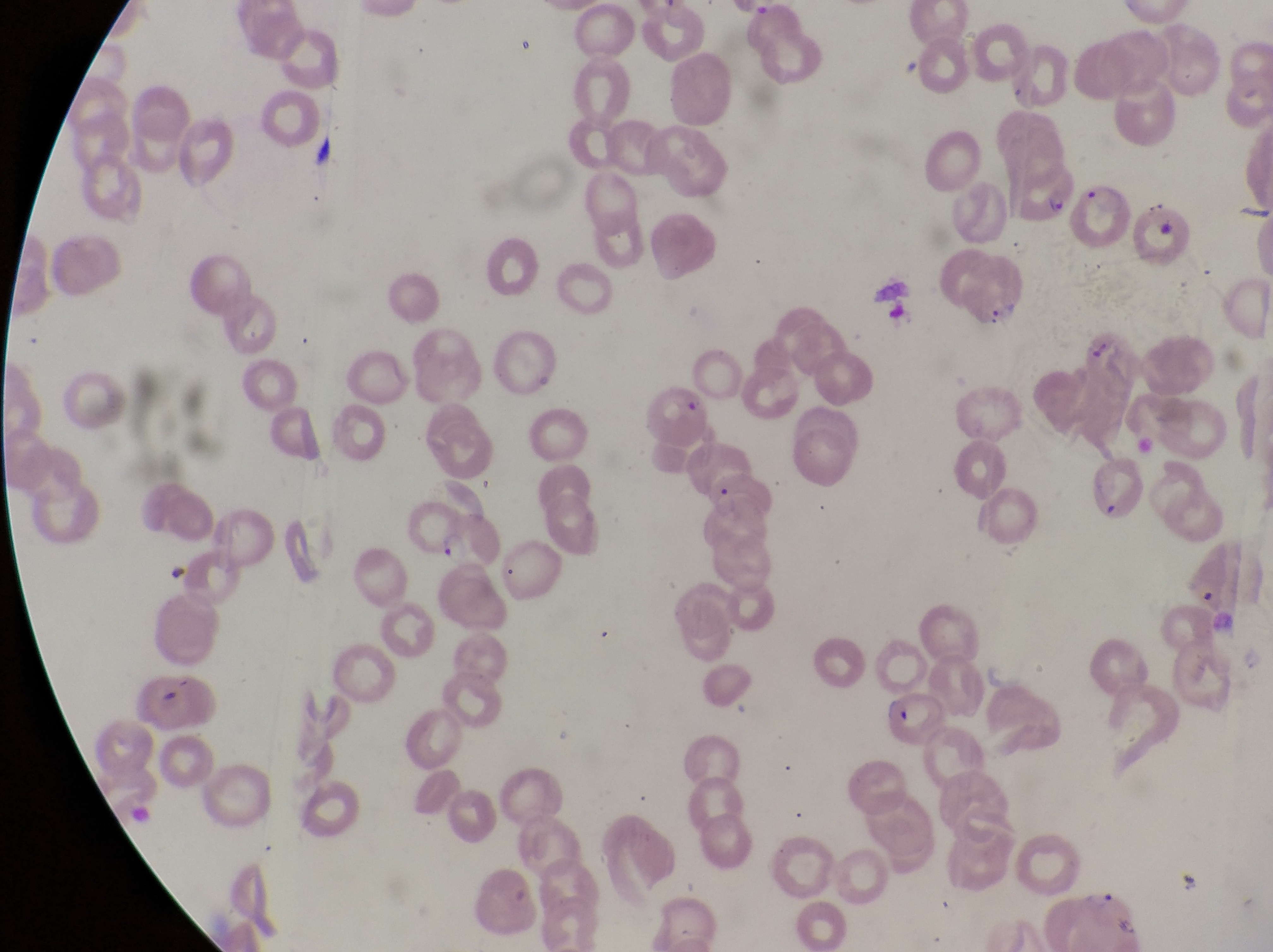
Approximate bounding boxes as (left, top, right, bottom) in pixels.
Summary:
  - Parasitised red blood cell locations: (1011, 158, 1081, 225), (1081, 180, 1138, 250), (961, 248, 1036, 324), (882, 692, 949, 752)
  - Trophozoite locations: (442, 530, 470, 569)
  - Preparation: thin blood film
  - Magnification: 1000x
  - Capture: smartphone photograph through the eyepiece of an Olympus CX-23 microscope
  - Country: Uganda
  - Image size: 1273×952 pixels
  - Field of view: single